State which parasite is depicted.
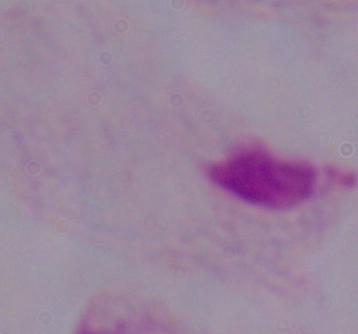
This is a trichomonad.

{
  "modality": "photomicrograph",
  "magnification": "1000x"
}